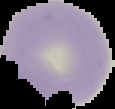 Cell region segmented out of the field of view; the surrounding area is masked to black. Image is 115×109 pixels. From a thin blood smear. Malaria status: uninfected.